Identify the blood parasite species.
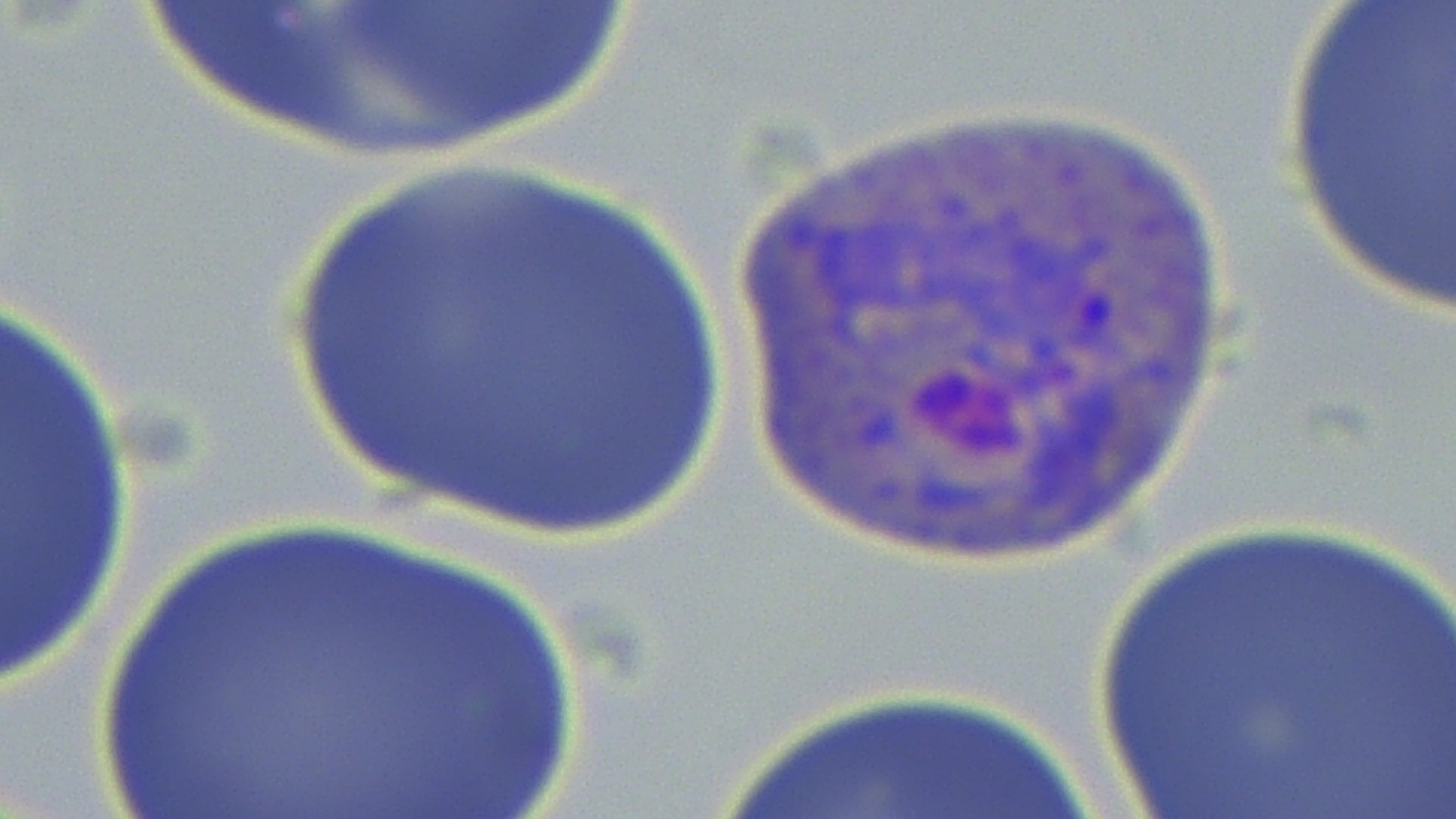

Plasmodium vivax.

stain = May-Grünwald-Giemsa
uninfected red blood cell locations = approximate bounding boxes as (x1,y1)-(x2,y2) corner pairs in pixels: (1277,0)-(1456,322), (279,157)-(722,536), (0,303)-(147,695), (66,504)-(608,819), (1076,510)-(1456,819)
preparation = thin blood smear
image size = 1456×819 pixels
modality = optical microscopy
magnification = 1000x
Plasmodium vivax-infected red blood cell locations = approximate bounding boxes as (x1,y1)-(x2,y2) corner pairs in pixels: (713,96)-(1252,564)
field of view = single